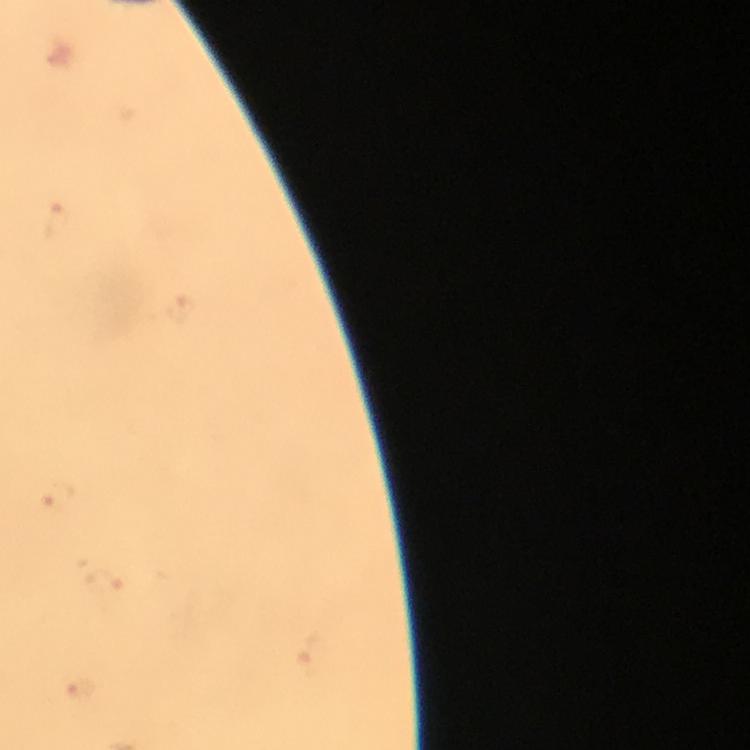
Approximate object centers, in pixels from the top-left corner.
Summary:
  - Malaria parasite locations: (x=177, y=306), (x=52, y=499), (x=102, y=581)
  - Immersion oil: applied
  - Stain: Giemsa
  - Preparation: thick blood smear
  - Capture: smartphone camera through the microscope
  - Image size: 750×750 pixels
  - Context: from a malaria diagnostic workup
  - Magnification: 100x
  - Cropped from: one field of view